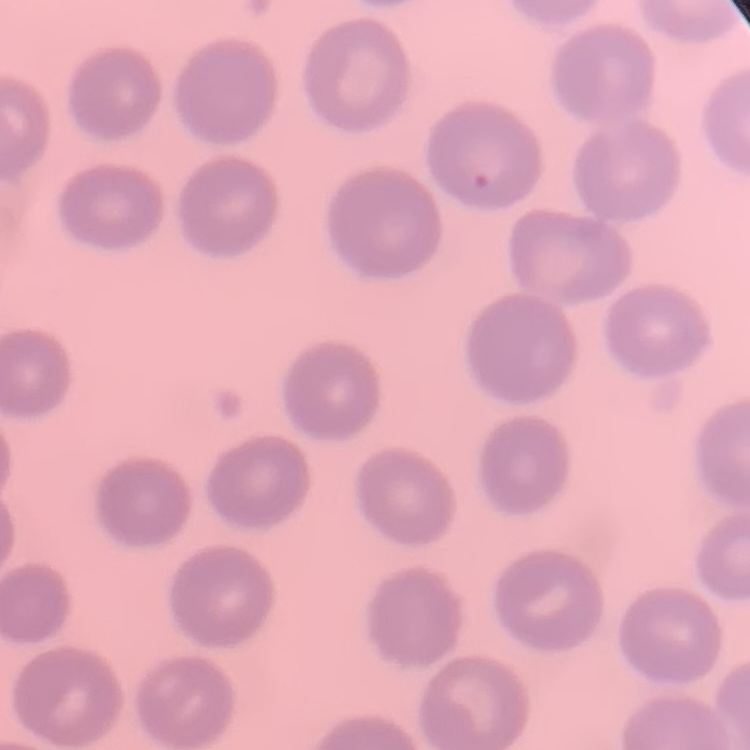
The erythrocytes show no rouleaux formation. Thin blood film. One tile cut from a larger photomicrograph. Stained with either Field's or Giemsa.